Assess the morphology of the erythrocytes.
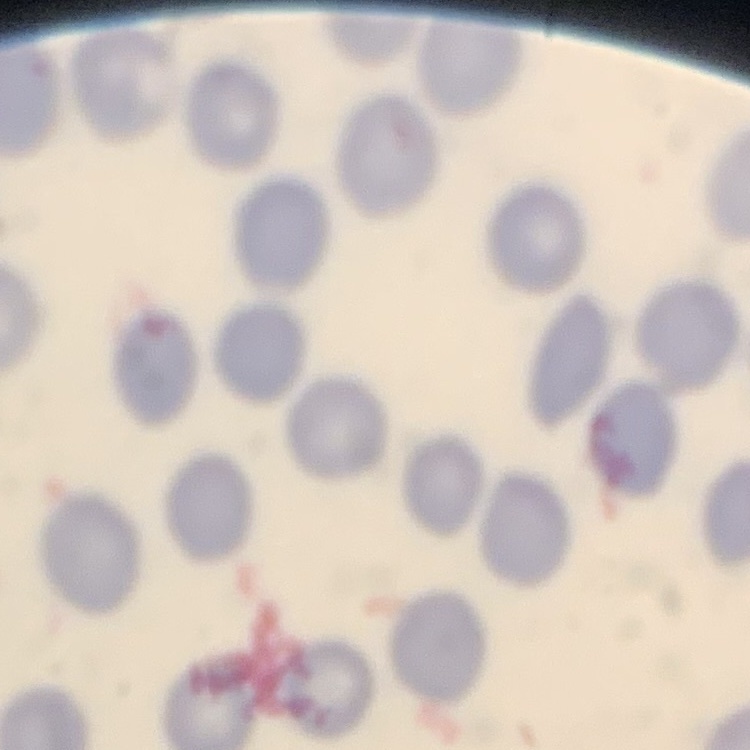

No rouleaux formation.

image type = one tile cut from a larger photomicrograph
preparation = thin peripheral smear
stain = Field's or Giemsa